Describe the morphology of the erythrocytes.
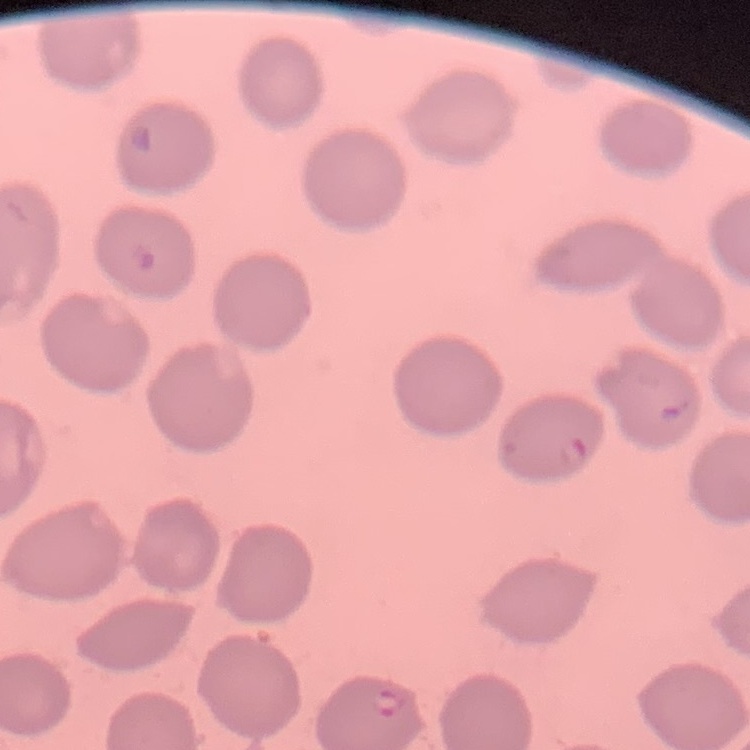
They show no rouleaux formation.

Summary:
  - Image type: one tile cut from a larger photomicrograph
  - Preparation: thin blood smear
  - Stain: Field's or Giemsa